Locate every malaria parasite.
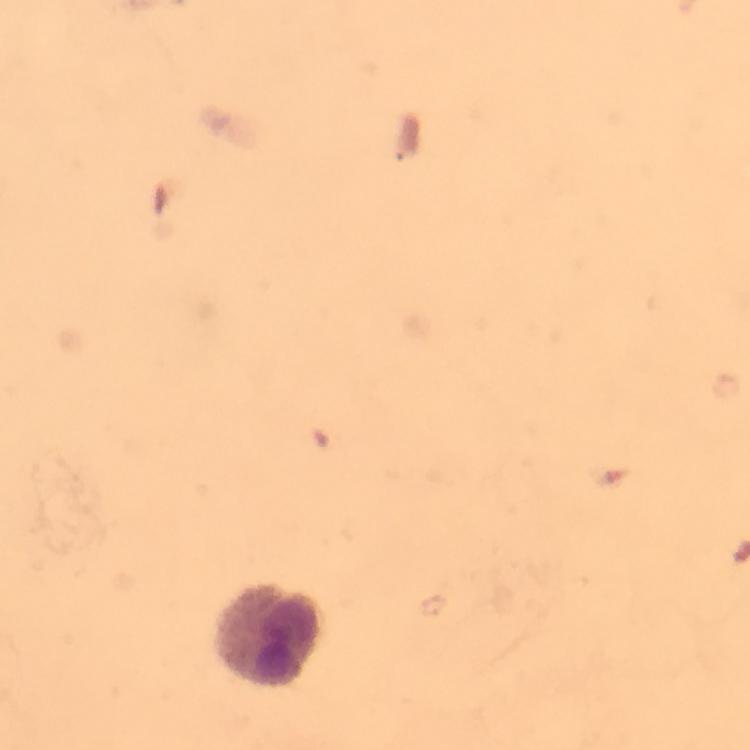
No malaria parasites seen.

Approximate object centers, in pixels from the top-left corner. Leukocyte locations: (x=269, y=637). From a diagnostic examination for malaria. Cropped region of a single field of view. Image is 750×750 pixels. Thick blood film. Photographed through the microscope with a smartphone camera. Immersion oil was used. At 100x magnification. Giemsa stain.